Report the malaria status of this cell.
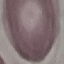

Uninfected.

Summary:
  - Capture: smartphone camera at the microscope eyepiece
  - Image type: automatically extracted cell patch, resized to 64 × 64 pixels
  - Preparation: thin blood smear
  - Stain: Giemsa